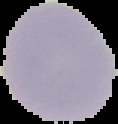 Image is 118×124 pixels. From a thin blood film. Malaria status: uninfected. Cell region segmented out of the field of view; the surrounding area is masked to black.